Assess this cell for malaria.
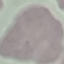
It is uninfected.

image_type: cell patch, automatically extracted from a larger field of view and resized to 64 × 64 pixels
capture: smartphone camera at the microscope eyepiece
stain: Giemsa
preparation: thin smear